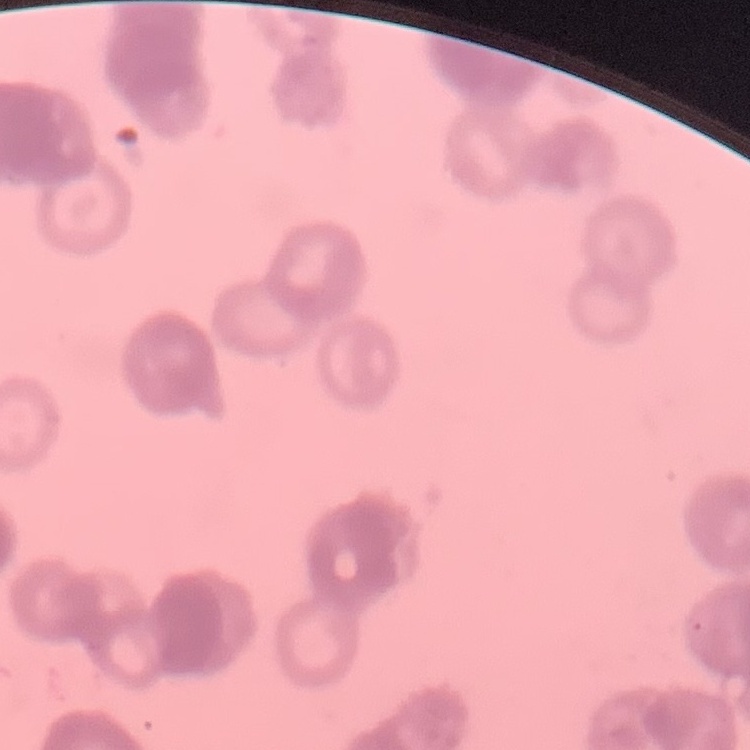

Summary:
  - Red blood cell morphology: rouleaux formation
  - Image type: one tile cut from a larger photomicrograph
  - Preparation: thin peripheral smear
  - Stain: Field's or Giemsa